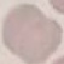 Result: no malaria parasites detected. Acquired by smartphone through the microscope eyepiece. Giemsa stain. Thin blood film. Cell patch, automatically extracted from a larger field of view and resized to 64 × 64 pixels.